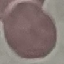
Malaria status: uninfected. Photographed with a smartphone camera at the microscope eyepiece. Automatically extracted cell patch, resized to 64 × 64 pixels. Thin blood smear. Giemsa stain.